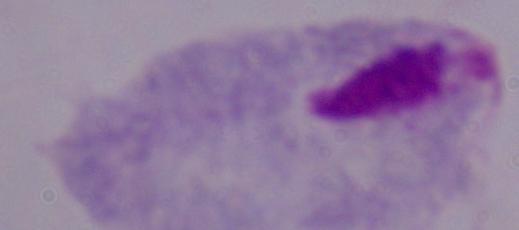
Summary:
  - Identification: trichomonad
  - Modality: micrograph
  - Magnification: 1000x